Identify the blood parasite species.
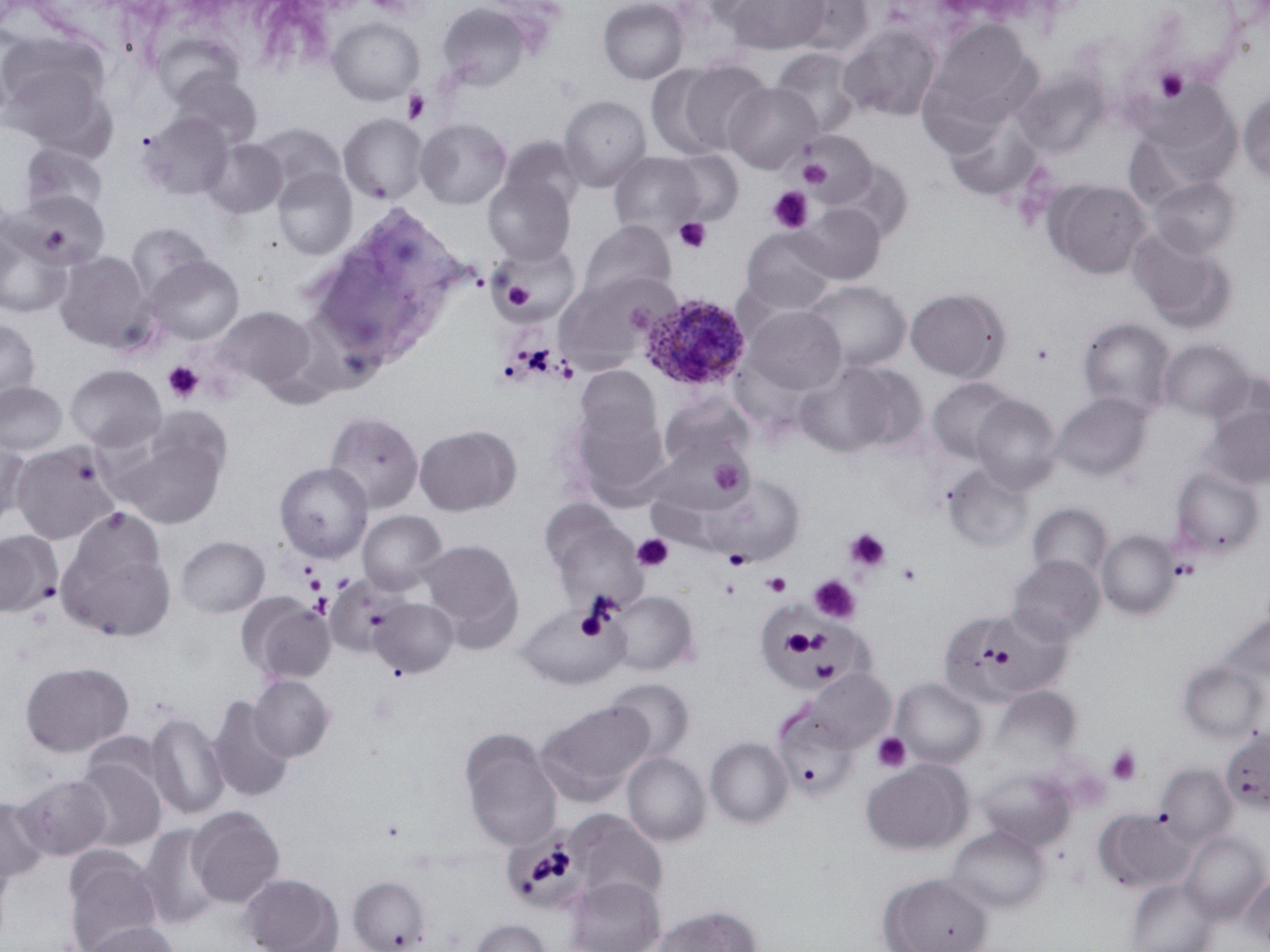
Plasmodium ovale.

Approximate bounding boxes as named x1/y1/x2/y2 corners in pixels. Plasmodium ovale-infected red blood cell locations: (x1=638, y1=292, x2=751, y2=393). Uninfected red blood cell locations: (x1=598, y1=0, x2=688, y2=84), (x1=726, y1=0, x2=831, y2=55), (x1=784, y1=0, x2=875, y2=58), (x1=437, y1=2, x2=531, y2=92), (x1=327, y1=16, x2=425, y2=106), (x1=923, y1=19, x2=1039, y2=130), (x1=838, y1=25, x2=943, y2=123), (x1=153, y1=33, x2=244, y2=109), (x1=0, y1=34, x2=115, y2=149), (x1=771, y1=48, x2=862, y2=140), (x1=674, y1=59, x2=771, y2=156), (x1=646, y1=65, x2=733, y2=160), (x1=1014, y1=69, x2=1108, y2=156), (x1=167, y1=71, x2=263, y2=150), (x1=1135, y1=80, x2=1239, y2=176), (x1=724, y1=83, x2=821, y2=174), (x1=1238, y1=90, x2=1270, y2=186), (x1=558, y1=95, x2=652, y2=192), (x1=943, y1=111, x2=1042, y2=201), (x1=142, y1=112, x2=236, y2=200), (x1=338, y1=112, x2=428, y2=205), (x1=415, y1=117, x2=511, y2=209), (x1=252, y1=122, x2=346, y2=200), (x1=796, y1=130, x2=876, y2=207), (x1=500, y1=137, x2=586, y2=215), (x1=201, y1=138, x2=287, y2=219), (x1=19, y1=141, x2=109, y2=219), (x1=666, y1=150, x2=744, y2=227), (x1=608, y1=151, x2=705, y2=239), (x1=827, y1=159, x2=914, y2=243), (x1=272, y1=167, x2=357, y2=260), (x1=483, y1=174, x2=575, y2=264), (x1=1147, y1=176, x2=1240, y2=259), (x1=1043, y1=179, x2=1151, y2=279), (x1=13, y1=190, x2=110, y2=271), (x1=796, y1=203, x2=887, y2=284), (x1=578, y1=220, x2=676, y2=304), (x1=0, y1=222, x2=73, y2=319), (x1=125, y1=223, x2=214, y2=303), (x1=739, y1=227, x2=837, y2=316), (x1=1127, y1=228, x2=1237, y2=333), (x1=488, y1=245, x2=574, y2=325), (x1=55, y1=251, x2=152, y2=352), (x1=144, y1=255, x2=245, y2=345), (x1=554, y1=274, x2=665, y2=373), (x1=802, y1=280, x2=911, y2=373), (x1=905, y1=287, x2=1010, y2=382), (x1=745, y1=305, x2=846, y2=398), (x1=212, y1=306, x2=318, y2=395), (x1=1078, y1=317, x2=1177, y2=419), (x1=0, y1=318, x2=41, y2=406), (x1=1158, y1=339, x2=1253, y2=422), (x1=794, y1=361, x2=919, y2=456), (x1=65, y1=364, x2=166, y2=452), (x1=574, y1=366, x2=663, y2=453), (x1=927, y1=377, x2=1017, y2=463), (x1=0, y1=381, x2=67, y2=456), (x1=1052, y1=392, x2=1152, y2=482), (x1=660, y1=394, x2=753, y2=470), (x1=971, y1=394, x2=1062, y2=492), (x1=568, y1=395, x2=670, y2=506), (x1=1201, y1=402, x2=1270, y2=491), (x1=324, y1=410, x2=424, y2=513), (x1=109, y1=421, x2=229, y2=529), (x1=414, y1=424, x2=521, y2=516), (x1=0, y1=437, x2=30, y2=530), (x1=10, y1=440, x2=120, y2=545), (x1=657, y1=442, x2=752, y2=513), (x1=273, y1=462, x2=373, y2=563), (x1=942, y1=463, x2=1033, y2=551), (x1=1169, y1=465, x2=1265, y2=560), (x1=711, y1=475, x2=805, y2=565), (x1=1027, y1=503, x2=1113, y2=582), (x1=540, y1=504, x2=645, y2=612), (x1=357, y1=510, x2=447, y2=594), (x1=57, y1=529, x2=176, y2=644), (x1=1096, y1=529, x2=1181, y2=620), (x1=0, y1=531, x2=61, y2=617), (x1=176, y1=535, x2=270, y2=617), (x1=418, y1=538, x2=524, y2=651), (x1=1007, y1=555, x2=1104, y2=646), (x1=608, y1=590, x2=698, y2=675), (x1=238, y1=593, x2=335, y2=683), (x1=369, y1=597, x2=458, y2=679), (x1=517, y1=603, x2=627, y2=690), (x1=940, y1=607, x2=1068, y2=707), (x1=1217, y1=611, x2=1270, y2=688), (x1=1177, y1=659, x2=1268, y2=743), (x1=19, y1=661, x2=134, y2=758), (x1=801, y1=668, x2=895, y2=753), (x1=247, y1=675, x2=335, y2=762), (x1=605, y1=678, x2=694, y2=762), (x1=891, y1=678, x2=986, y2=769), (x1=990, y1=687, x2=1080, y2=767), (x1=207, y1=696, x2=295, y2=802), (x1=535, y1=699, x2=653, y2=805), (x1=773, y1=708, x2=859, y2=801), (x1=145, y1=712, x2=229, y2=821), (x1=458, y1=727, x2=563, y2=852), (x1=1220, y1=730, x2=1270, y2=815), (x1=705, y1=737, x2=794, y2=828), (x1=622, y1=752, x2=710, y2=847), (x1=73, y1=756, x2=167, y2=852), (x1=861, y1=758, x2=973, y2=855), (x1=1154, y1=763, x2=1237, y2=848), (x1=977, y1=768, x2=1076, y2=851), (x1=14, y1=774, x2=112, y2=861), (x1=0, y1=795, x2=49, y2=884), (x1=186, y1=805, x2=286, y2=908), (x1=1093, y1=809, x2=1195, y2=893), (x1=569, y1=811, x2=667, y2=906), (x1=139, y1=825, x2=224, y2=930), (x1=946, y1=825, x2=1050, y2=913), (x1=1180, y1=831, x2=1269, y2=925), (x1=62, y1=846, x2=164, y2=952), (x1=1240, y1=868, x2=1270, y2=948), (x1=240, y1=872, x2=344, y2=952), (x1=878, y1=872, x2=994, y2=952), (x1=347, y1=875, x2=431, y2=952), (x1=565, y1=875, x2=665, y2=952), (x1=1126, y1=877, x2=1218, y2=952), (x1=653, y1=904, x2=762, y2=952), (x1=470, y1=917, x2=552, y2=952), (x1=82, y1=922, x2=179, y2=952). Platelet locations: (x1=366, y1=0, x2=416, y2=17), (x1=1154, y1=67, x2=1188, y2=102), (x1=402, y1=89, x2=430, y2=123), (x1=795, y1=133, x2=872, y2=203), (x1=798, y1=157, x2=832, y2=189), (x1=767, y1=186, x2=815, y2=234), (x1=673, y1=217, x2=712, y2=253), (x1=501, y1=278, x2=535, y2=313), (x1=512, y1=343, x2=558, y2=379), (x1=162, y1=360, x2=204, y2=404), (x1=700, y1=453, x2=753, y2=502), (x1=845, y1=527, x2=890, y2=573), (x1=632, y1=534, x2=673, y2=572), (x1=723, y1=548, x2=751, y2=570), (x1=1170, y1=557, x2=1198, y2=581), (x1=896, y1=562, x2=922, y2=587), (x1=762, y1=572, x2=792, y2=596), (x1=302, y1=573, x2=325, y2=594), (x1=331, y1=573, x2=354, y2=593), (x1=809, y1=575, x2=861, y2=623), (x1=719, y1=578, x2=741, y2=599), (x1=309, y1=592, x2=332, y2=618), (x1=781, y1=628, x2=818, y2=657), (x1=872, y1=732, x2=910, y2=772), (x1=1106, y1=744, x2=1143, y2=785). Single field of view. 1000x magnification. Light microscopy. Thin blood smear. Image is 1270×952 pixels. May-Grünwald-Giemsa-stained preparation.